Locate every malaria parasite.
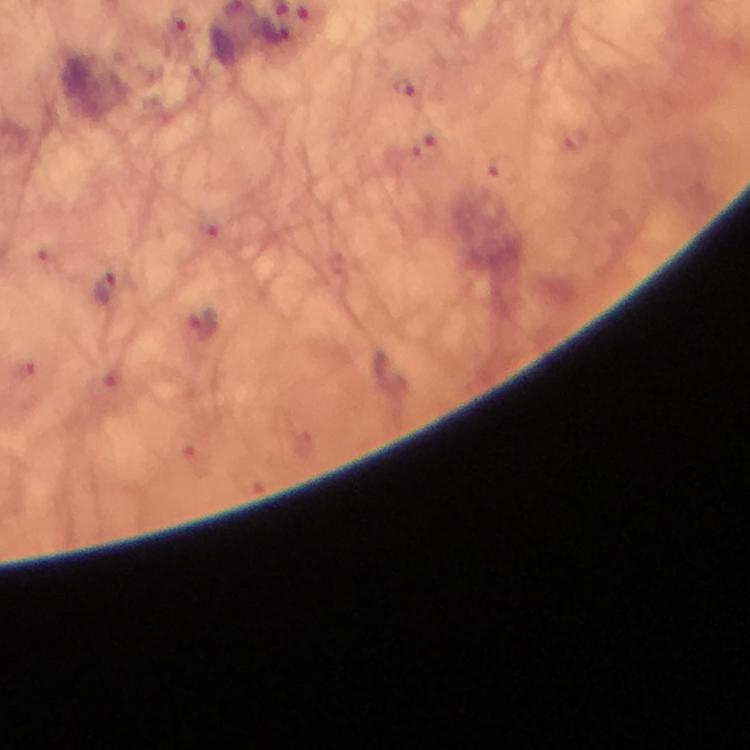
Approximate centers as {x, y} in pixels.
Malaria parasites: {276, 34}, {406, 87}, {108, 287}.

capture = smartphone camera through the microscope
immersion oil = used
cropped from = a single field of view
context = from a diagnostic examination for malaria
image size = 750×750 pixels
stain = Giemsa
magnification = 100x
preparation = thick smear